Classify this cell by malaria status.
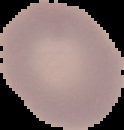

Uninfected.

preparation = thin blood film
image type = segmented cell region on a black background
image size = 124×130 pixels